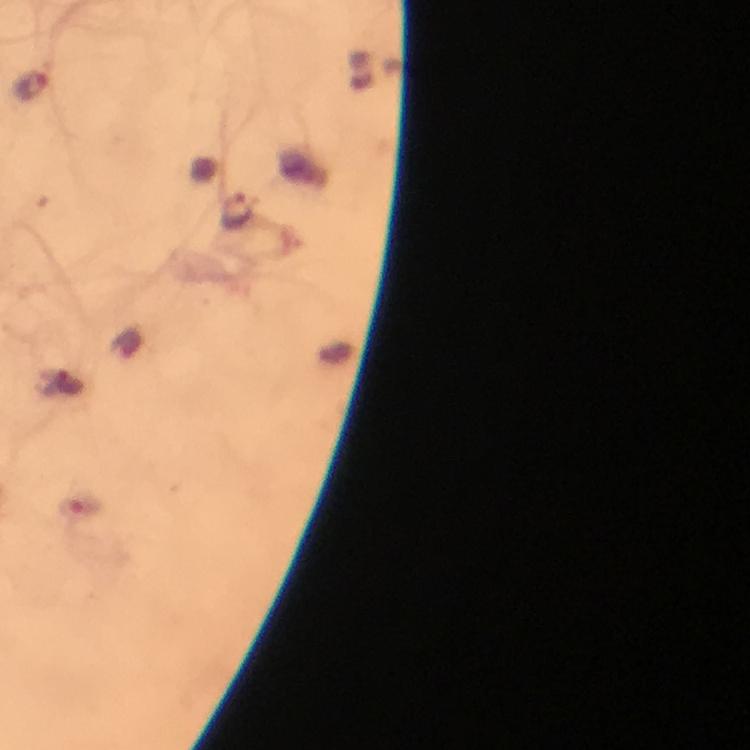
preparation = thick smear
magnification = 100x
malaria parasite locations = approximate centers as {x, y} in pixels: {33, 86}, {237, 211}
image size = 750×750 pixels
cropped from = a single field of view
immersion oil = used
capture = smartphone mounted on the microscope
stain = Giemsa
context = from a malaria diagnostic workup